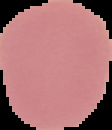
{
  "malaria_status": "uninfected",
  "image_size": "112×130 pixels",
  "image_type": "cell region segmented out of the field of view; surrounding area masked to black",
  "preparation": "thin blood smear"
}